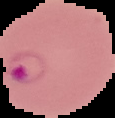
result = Plasmodium parasites detected
preparation = thin blood film
image size = 115×118 pixels
image type = cell region segmented out of the field of view; surrounding area masked to black